Assess this cell for malaria.
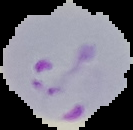
Parasitized.

The area outside the segmented cell region is set to black. Image is 133×130 pixels. From a thin blood smear.